State which parasite is depicted.
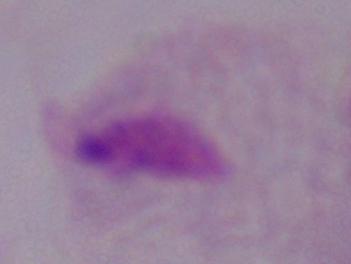
A trichomonad.

magnification = 1000x
modality = photomicrograph